Report the malaria status of this cell.
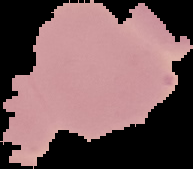
Uninfected.

image_type: segmented cell region on a black background
preparation: thin blood smear
image_size: 193×169 pixels